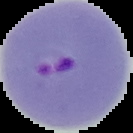
From a thin blood film. Segmented cell region on a black background. Image is 133×133 pixels. Malaria status: parasitized.